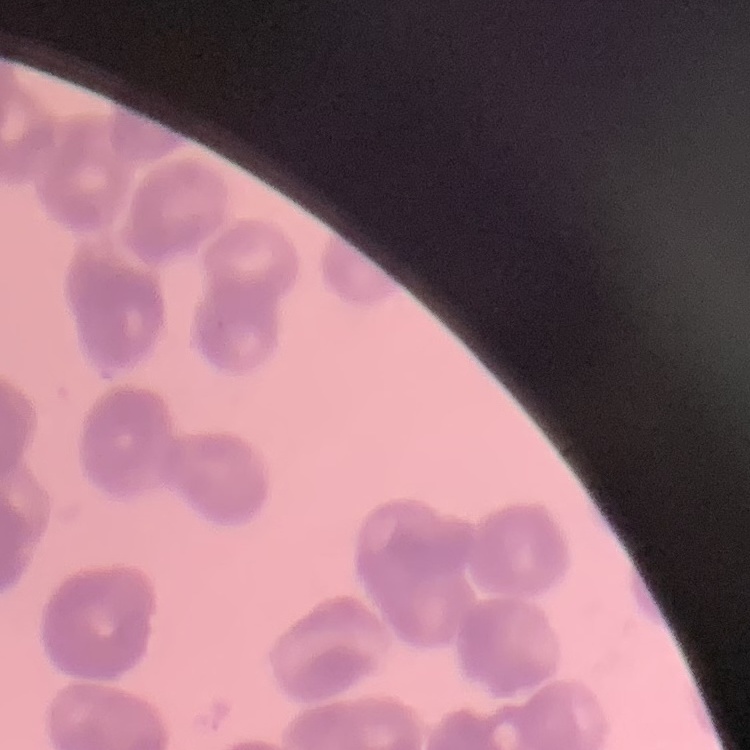

red blood cell morphology = rouleaux formation
preparation = thin blood film
stain = Field's or Giemsa
image type = one tile cut from a larger photomicrograph